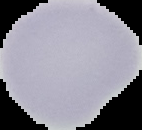
preparation = thin blood film
image size = 142×130 pixels
result = negative for Plasmodium parasites
image type = cell region segmented out of the field of view; surrounding area masked to black